Describe the morphology of the erythrocytes.
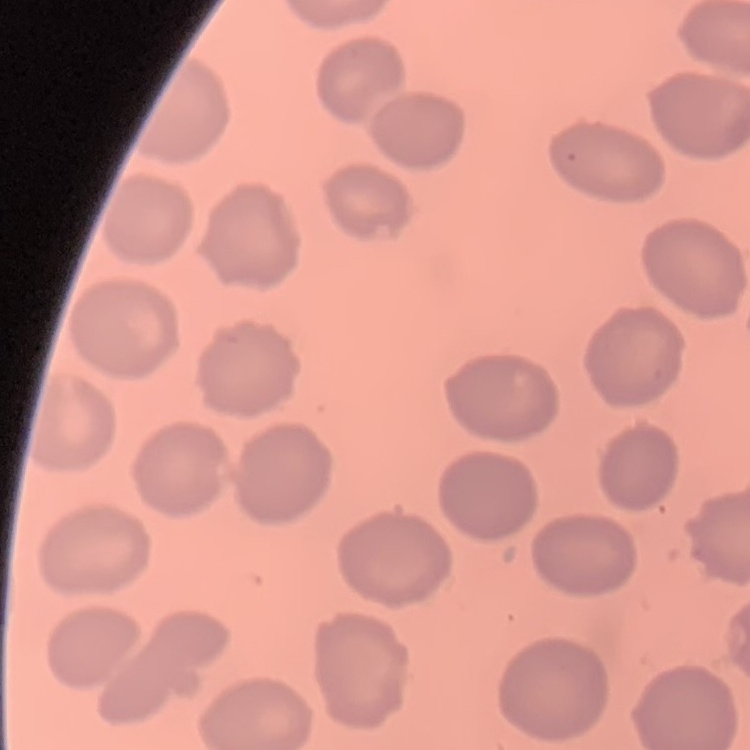
They show no rouleaux formation.

Square crop of a larger photomicrograph. Field's or Giemsa stain. Thin blood smear.